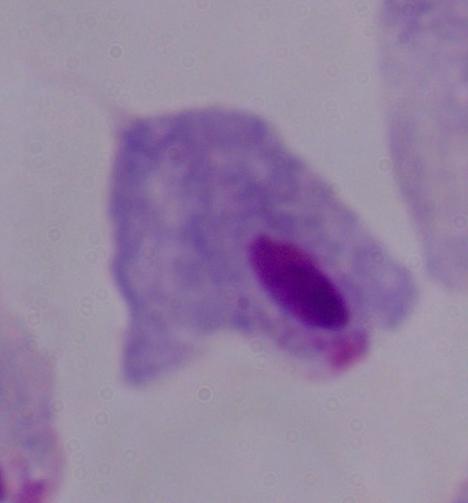

A trichomonad is shown. Captured at 1000x magnification. Photomicrograph.